Mark where platelets are.
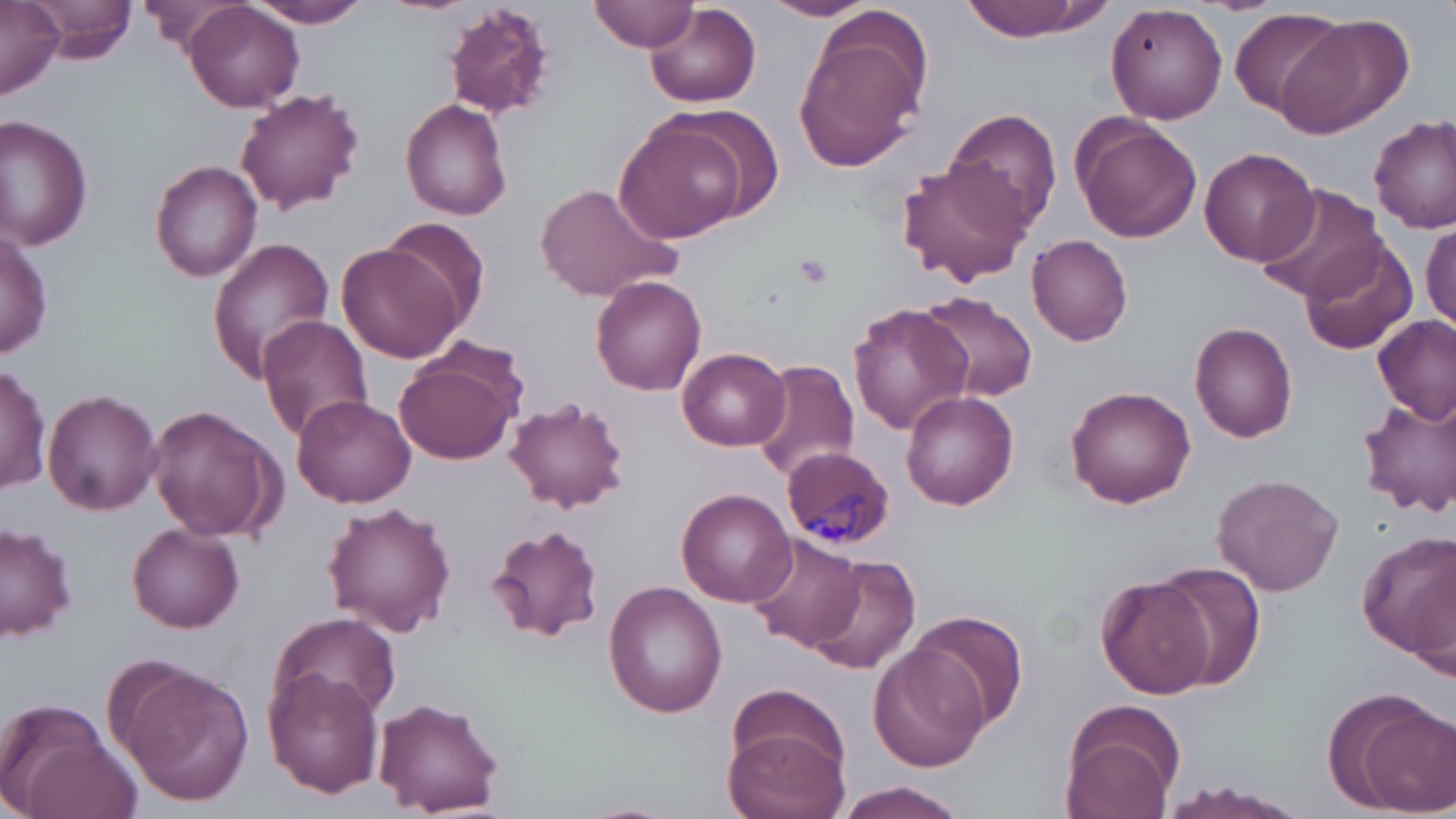
Approximate bounding boxes as [x1, y1, x2, y2] in pixels.
Platelets: [794, 251, 835, 289].

Plasmodium malariae-infected red blood cell locations: [782, 446, 896, 549]. Uninfected red blood cell locations: [29, 0, 138, 63], [138, 0, 252, 52], [245, 0, 373, 28], [378, 0, 476, 15], [592, 0, 699, 52], [761, 0, 882, 21], [957, 0, 1103, 42], [443, 1, 556, 118], [0, 3, 65, 100], [185, 4, 304, 112], [1105, 4, 1229, 125], [646, 5, 760, 108], [1231, 7, 1347, 115], [1273, 15, 1408, 139], [792, 21, 930, 173], [235, 88, 365, 215], [401, 98, 514, 220], [944, 108, 1062, 231], [1369, 112, 1456, 233], [0, 114, 94, 254], [1072, 115, 1203, 244], [614, 117, 751, 244], [1199, 146, 1320, 266], [897, 157, 1032, 285], [151, 160, 263, 280], [536, 181, 677, 301], [1254, 185, 1388, 304], [377, 217, 494, 329], [1420, 220, 1456, 334], [0, 224, 52, 359], [1027, 234, 1135, 345], [1300, 234, 1416, 357], [207, 238, 337, 383], [339, 240, 469, 361], [590, 275, 707, 397], [915, 292, 1038, 402], [849, 303, 970, 437], [256, 314, 374, 443], [1374, 314, 1454, 424], [1188, 322, 1298, 442], [395, 344, 524, 465], [678, 347, 789, 451], [750, 359, 861, 479], [1, 364, 50, 494], [1064, 383, 1197, 508], [43, 388, 162, 515], [900, 390, 1019, 511], [290, 394, 418, 507], [1356, 395, 1456, 519], [505, 396, 631, 513], [147, 405, 284, 544], [1210, 473, 1345, 596], [675, 487, 795, 606], [322, 502, 456, 636], [0, 521, 78, 643], [127, 522, 245, 634], [486, 522, 604, 642], [1358, 534, 1456, 663], [746, 536, 866, 656], [803, 555, 920, 678], [1155, 561, 1266, 688], [1097, 574, 1216, 699], [603, 582, 727, 718], [910, 611, 1028, 733], [269, 613, 401, 719], [870, 643, 987, 772], [115, 665, 255, 806], [265, 667, 384, 798], [1325, 688, 1453, 814], [373, 696, 506, 816], [1059, 697, 1187, 818], [0, 699, 131, 819], [724, 720, 850, 819], [1159, 781, 1304, 817], [835, 784, 967, 819]. Slide-level diagnosis: Plasmodium malariae. May-Grünwald-Giemsa stain. 1000x magnification. Optical microscopy. Image is 1456×819 pixels. Single field of view. Thin blood smear.